Locate every blood parasite and identify its species.
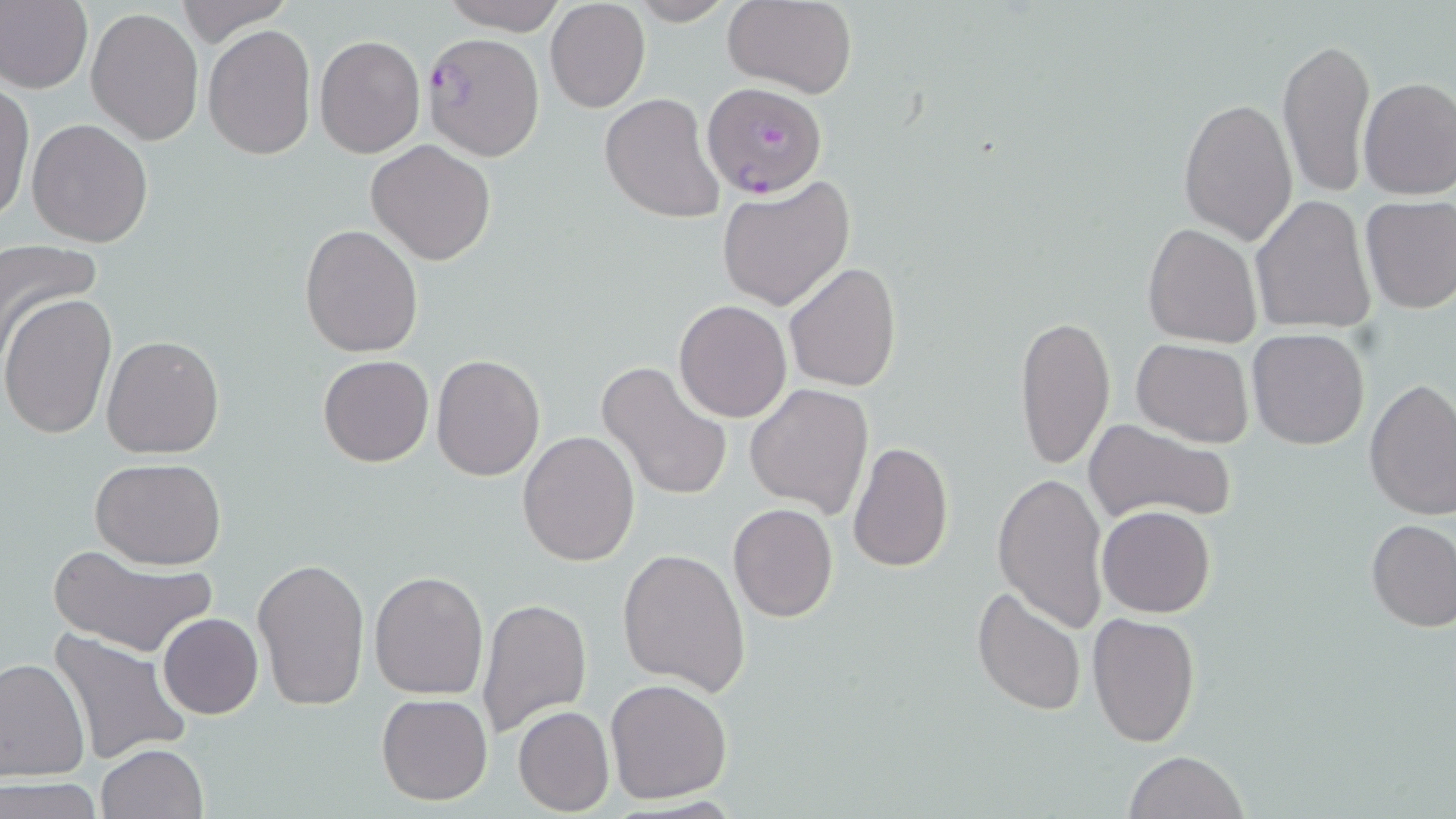

Approximate bounding boxes as (x1, y1, x2, y2) in pixels.
Plasmodium falciparum-infected red blood cells: (426, 32, 545, 158), (702, 81, 829, 199).
No Plasmodium ovale, Plasmodium malariae, Plasmodium vivax, Babesia divergens, or Trypanosoma brucei observed.

{
  "slide_level_diagnosis": "Plasmodium falciparum",
  "uninfected_red_blood_cell_locations": "approximate bounding boxes as (x1, y1, x2, y2) in pixels: (0, 0, 93, 95), (174, 0, 294, 43), (440, 0, 566, 32), (624, 0, 737, 25), (723, 0, 857, 97), (544, 1, 650, 113), (85, 6, 203, 146), (203, 24, 316, 161), (315, 35, 425, 157), (1277, 35, 1377, 200), (1357, 77, 1456, 200), (0, 81, 34, 226), (600, 92, 727, 224), (1178, 97, 1298, 246), (26, 118, 154, 247), (366, 140, 496, 265), (716, 177, 855, 312), (1359, 194, 1456, 314), (1250, 195, 1377, 335), (299, 223, 423, 359), (1143, 223, 1263, 347), (0, 240, 103, 359), (784, 261, 902, 394), (2, 292, 116, 440), (674, 299, 792, 423), (1015, 313, 1115, 470), (1248, 329, 1370, 450), (101, 334, 226, 460), (1132, 339, 1255, 448), (317, 354, 433, 467), (431, 354, 545, 481), (597, 360, 732, 503), (1363, 379, 1456, 523), (744, 382, 873, 517), (1083, 417, 1237, 527), (517, 430, 640, 565), (847, 441, 954, 574), (91, 459, 225, 570), (993, 471, 1108, 632), (727, 501, 841, 622), (1097, 505, 1216, 617), (1366, 519, 1456, 632), (48, 544, 218, 659), (618, 547, 751, 695), (253, 557, 371, 713), (369, 571, 488, 700), (972, 587, 1086, 716), (477, 597, 592, 737), (1087, 612, 1201, 747), (158, 613, 264, 719), (45, 629, 191, 766), (0, 657, 88, 785), (605, 677, 732, 804), (375, 694, 493, 806), (514, 705, 614, 815), (95, 743, 210, 819), (1124, 750, 1249, 819), (2, 777, 104, 818)",
  "preparation": "thin blood smear",
  "image_size": "1456×819 pixels",
  "magnification": "1000x",
  "field_of_view": "single",
  "modality": "light microscopy",
  "stain": "May-Grünwald-Giemsa"
}